Assess the morphology of the red blood cells.
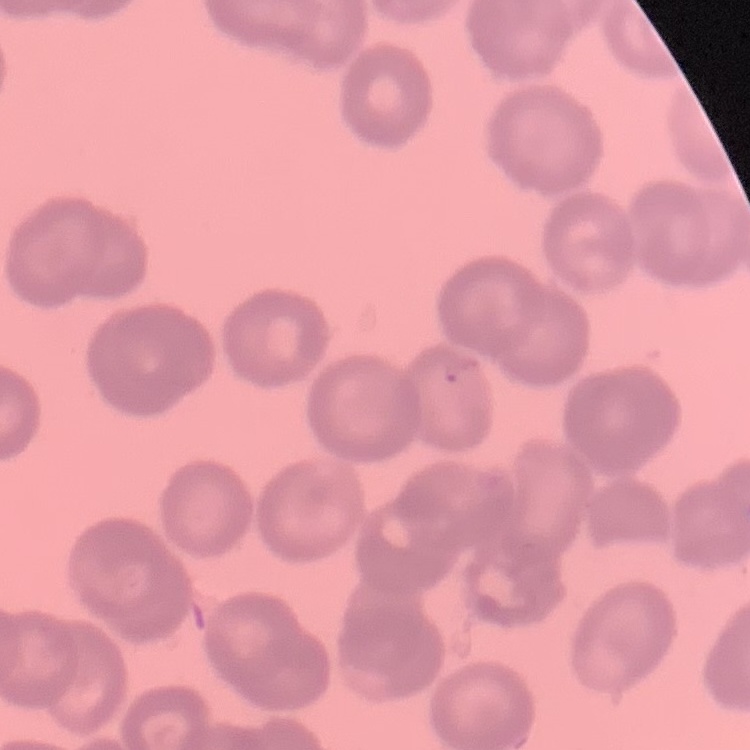

Rouleaux formation.

Summary:
  - Preparation: thin blood film
  - Stain: Field's or Giemsa
  - Image type: square crop of a larger photomicrograph